Outline each Plasmodium falciparum-infected red blood cell.
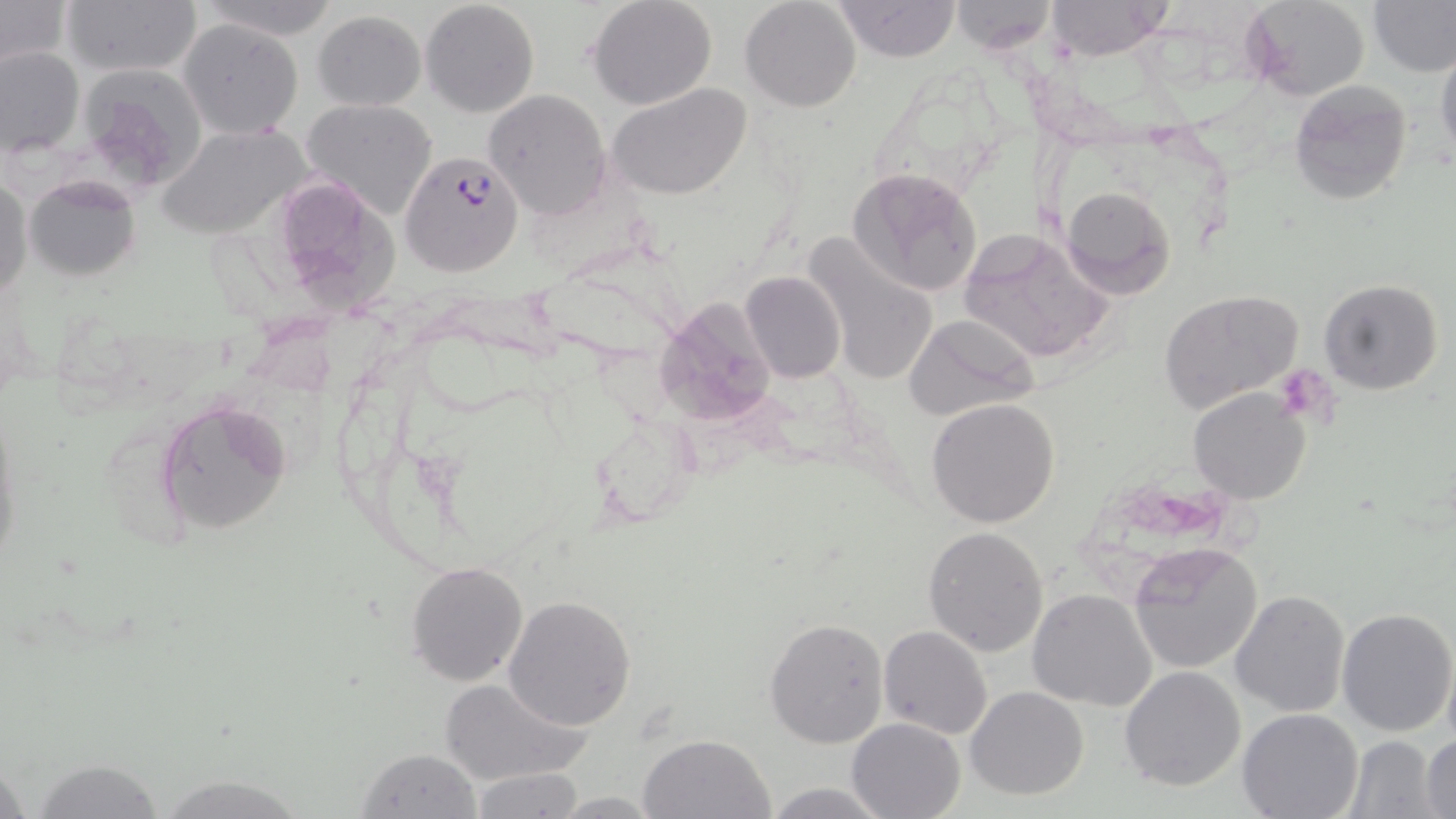

Approximate bounding boxes as (x1,y1)-(x2,y2) corner pairs in pixels.
Plasmodium falciparum-infected red blood cells: (399,149)-(525,277).

slide-level diagnosis = Plasmodium falciparum
platelet locations = approximate bounding boxes as (x1,y1)-(x2,y2) corner pairs in pixels: (1273,363)-(1335,428)
stain = May-Grünwald-Giemsa
magnification = 1000x
uninfected red blood cell locations = approximate bounding boxes as (x1,y1)-(x2,y2) corner pairs in pixels: (196,0)-(341,39), (420,0)-(540,118), (587,0)-(718,111), (739,0)-(861,113), (835,0)-(960,62), (1046,0)-(1172,61), (1240,0)-(1371,102), (1369,0)-(1455,76), (0,1)-(70,72), (61,1)-(201,78), (947,1)-(1058,54), (314,11)-(426,109), (179,20)-(304,140), (1433,43)-(1456,168), (0,46)-(85,157), (1289,80)-(1413,208), (607,83)-(751,201), (485,89)-(611,219), (305,99)-(436,219), (158,125)-(306,239), (848,167)-(983,298), (24,173)-(142,281), (1,176)-(32,301), (1058,184)-(1177,300), (959,228)-(1114,364), (798,231)-(943,388), (740,271)-(847,381), (1318,278)-(1444,396), (1160,288)-(1304,413), (652,297)-(778,429), (902,312)-(1041,420), (1188,387)-(1312,503), (926,397)-(1060,528), (157,399)-(294,536), (922,526)-(1050,657), (1128,541)-(1264,674), (407,560)-(528,686), (1028,589)-(1158,711), (1229,590)-(1350,717), (502,595)-(636,730), (1336,606)-(1456,738), (765,617)-(890,749), (880,625)-(993,741), (1119,665)-(1247,791), (439,675)-(591,785), (965,686)-(1090,800), (1236,709)-(1364,819), (845,718)-(965,819), (637,732)-(775,818), (1420,734)-(1455,818), (1344,735)-(1445,819), (357,748)-(482,819), (30,759)-(168,818), (466,767)-(588,818), (152,773)-(316,818), (761,780)-(894,818), (550,792)-(666,817)
field of view = one of a larger specimen
image size = 1456×819 pixels
preparation = thin blood film
modality = optical microscopy